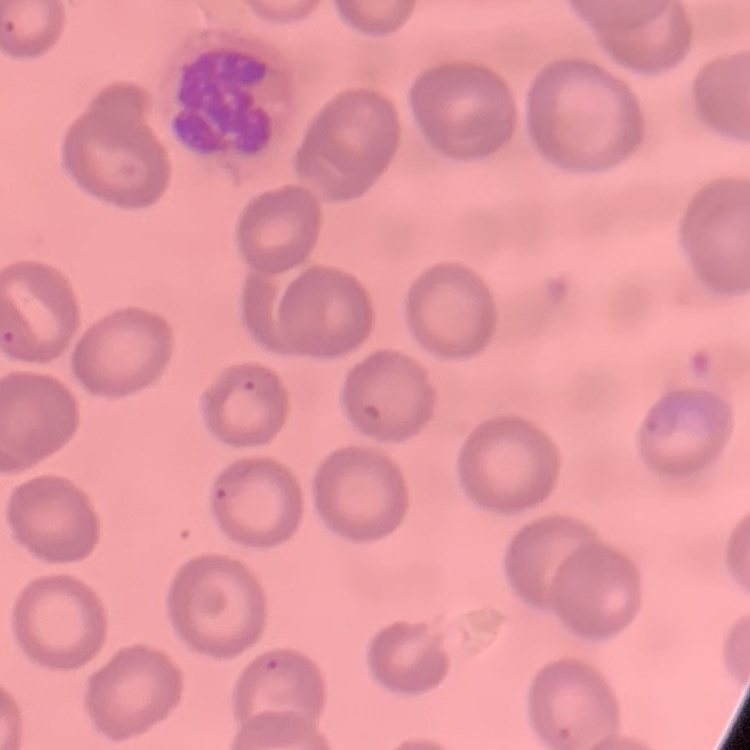 The erythrocytes exhibit no rouleaux formation. Thin blood smear. One tile cut from a larger photomicrograph. Field's or Giemsa stain.